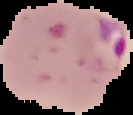
result = malaria parasites identified
preparation = thin blood film
image size = 133×115 pixels
image type = segmented cell region with the area outside set to black